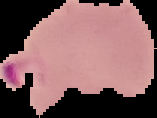

malaria status = parasitized
preparation = thin blood smear
image type = segmented cell region with the area outside set to black
image size = 157×118 pixels